Comment on the morphology of the erythrocytes.
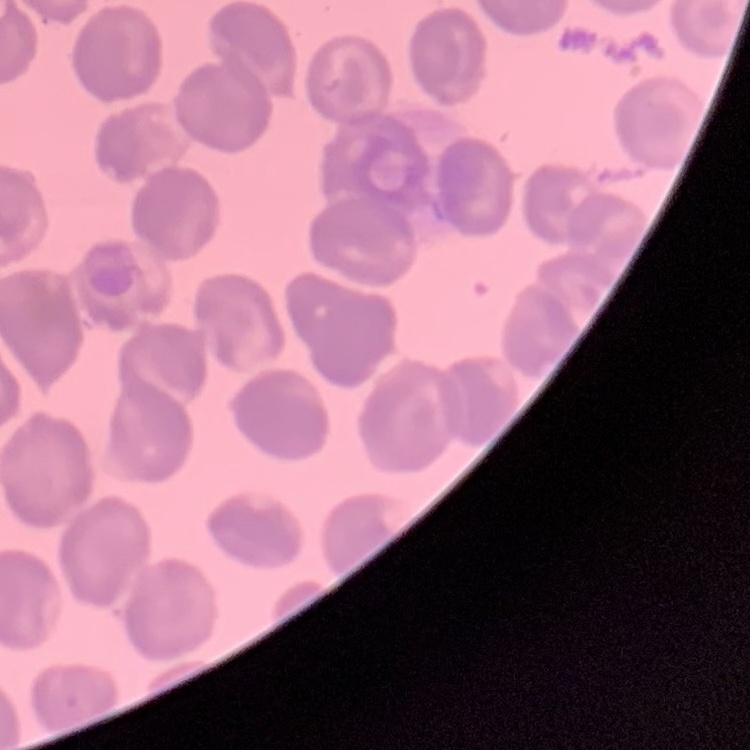
No rouleaux formation.

stain = Field's or Giemsa
preparation = thin blood film
image type = one tile cut from a larger photomicrograph